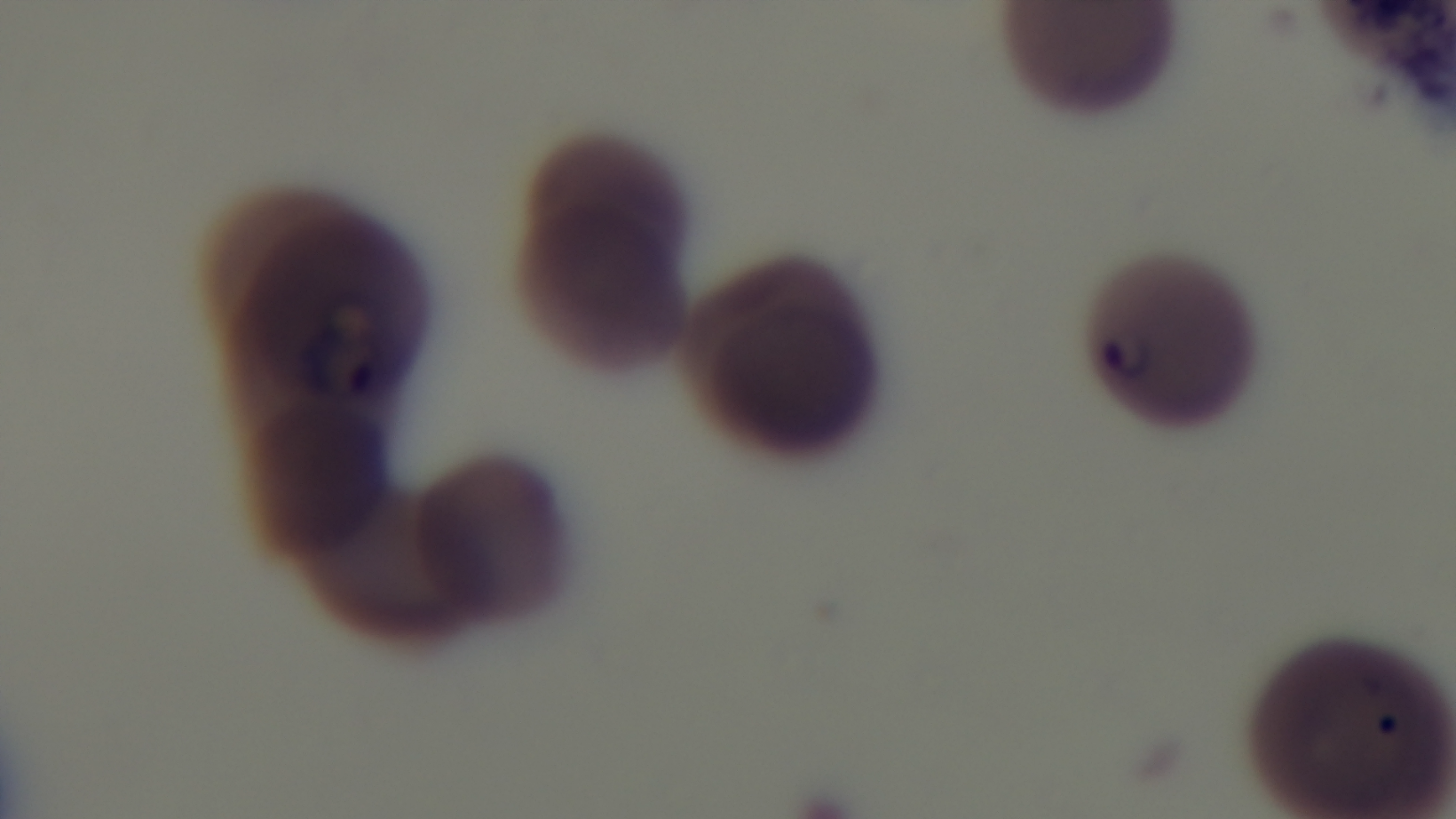

preparation = thin blood film
field of view = single
stain = Giemsa
capture = mounted 4K digital camera
malaria status = infected
modality = light microscopy
objective = 100x oil immersion